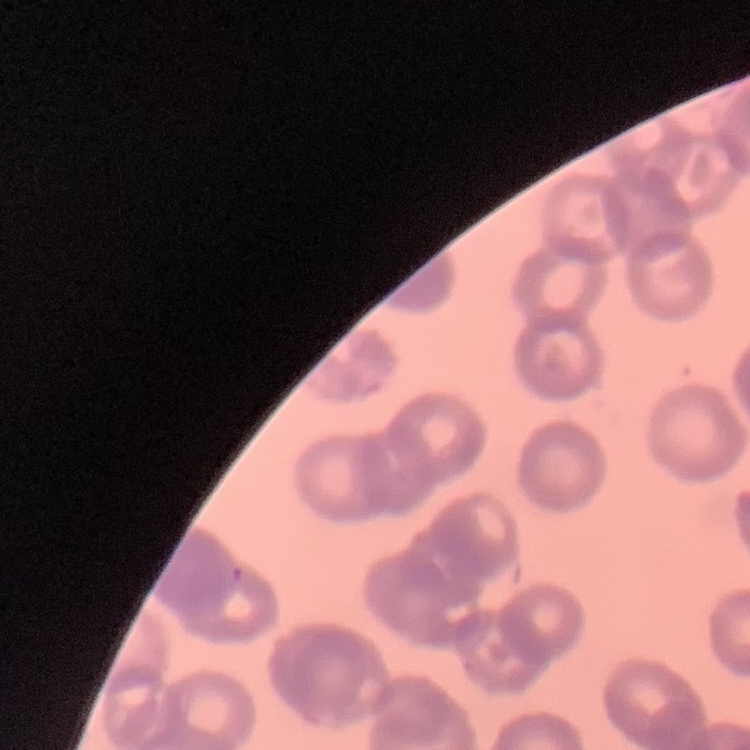
Summary:
  - Red blood cell morphology: rouleaux formation
  - Preparation: thin blood film
  - Image type: square crop of a larger photomicrograph
  - Stain: Field's or Giemsa